State which parasite is depicted.
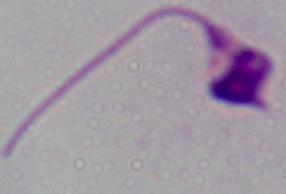

This is Leishmania.

Summary:
  - Modality: micrograph
  - Magnification: 1000x